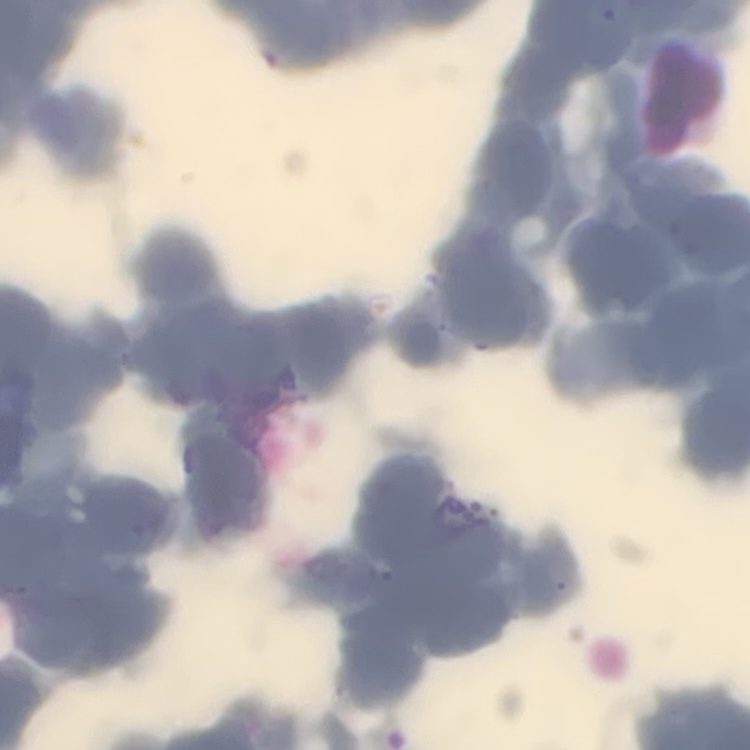

Summary:
  - Red blood cell morphology: rouleaux formation
  - Image type: square crop of a larger photomicrograph
  - Preparation: thin blood smear
  - Stain: Field's or Giemsa